Assess the morphology of the erythrocytes.
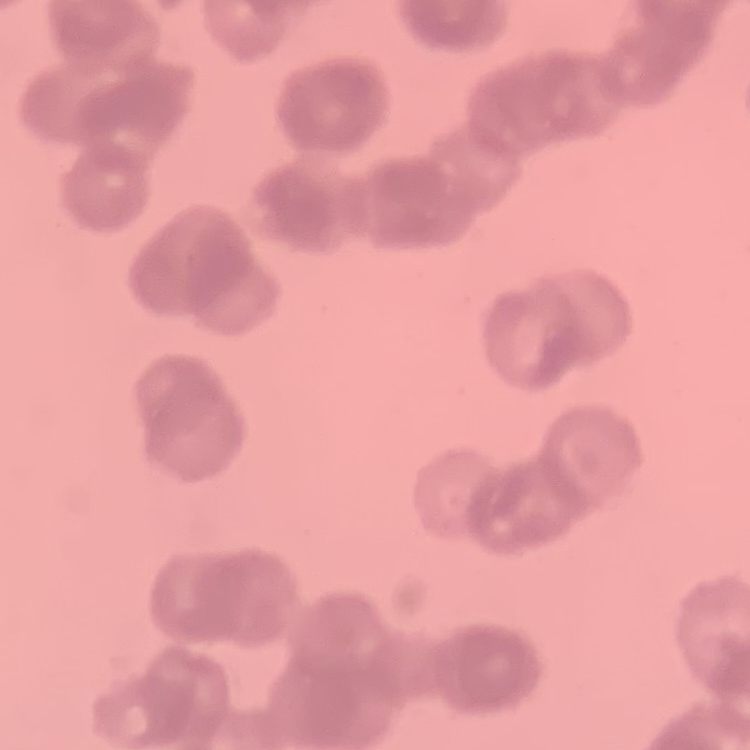
Rouleaux formation.

{
  "stain": "Field's or Giemsa",
  "image_type": "one tile cut from a larger photomicrograph",
  "preparation": "thin blood film"
}